Name the parasite shown.
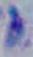
Toxoplasma gondii.

Summary:
  - Modality: micrograph
  - Magnification: 1000x